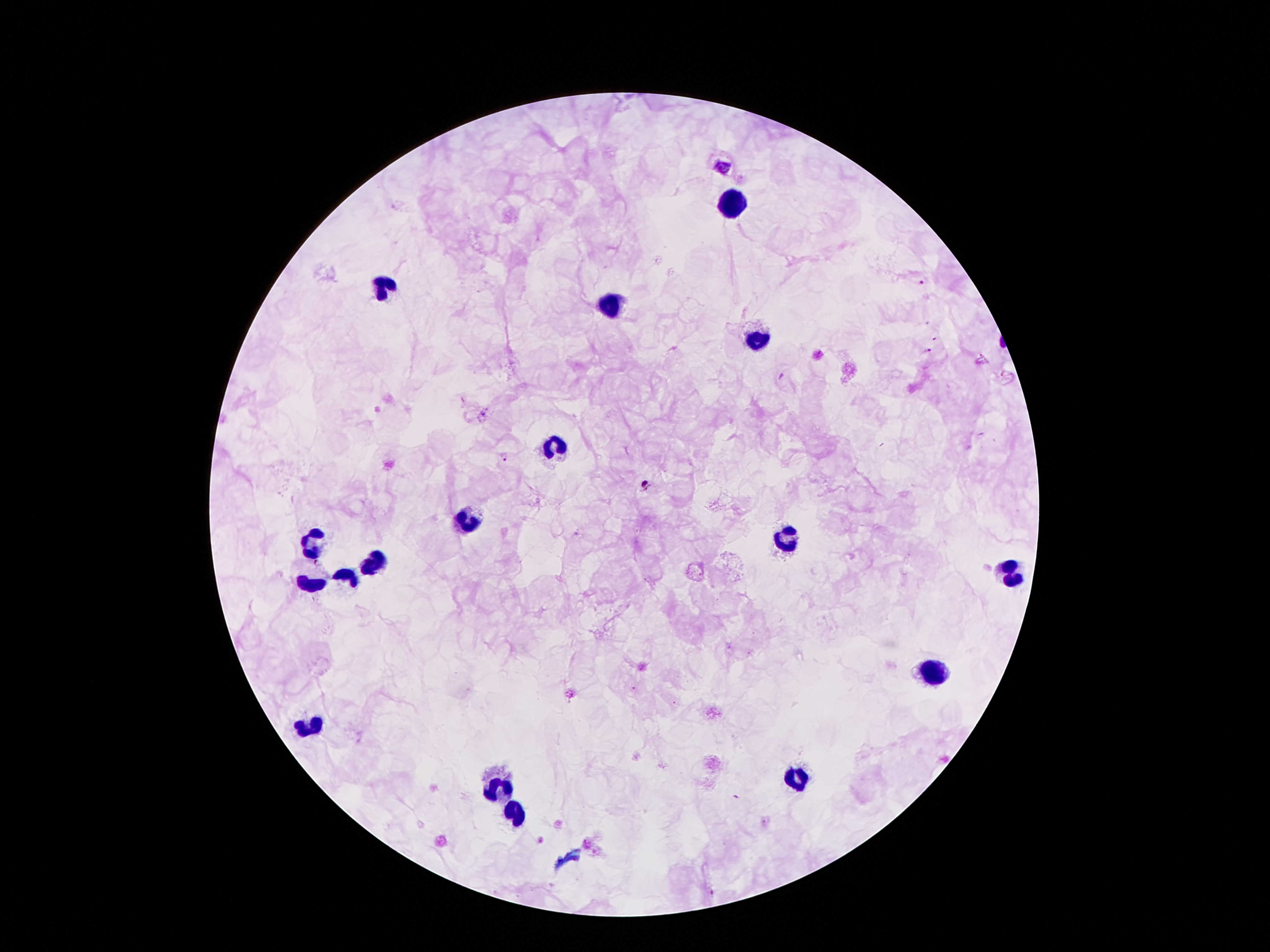
{
  "leukocyte_locations": "approximate centers as (x, y) in pixels: (732, 203), (383, 281), (611, 305), (758, 338), (555, 443), (464, 515), (783, 539), (312, 541), (372, 562), (1005, 571), (347, 575), (311, 583), (932, 671), (800, 775), (498, 788), (516, 812)",
  "patient_malaria_status": "infected with Plasmodium falciparum",
  "preparation": "thick blood smear",
  "magnification": "100x",
  "image_size": "1270×952 pixels",
  "malaria_parasite_locations": "approximate centers as (x, y) in pixels: (722, 168), (921, 284), (926, 352), (503, 456), (645, 484)",
  "capture": "smartphone through the microscope eyepiece",
  "stain": "Giemsa",
  "field_of_view": "single"
}